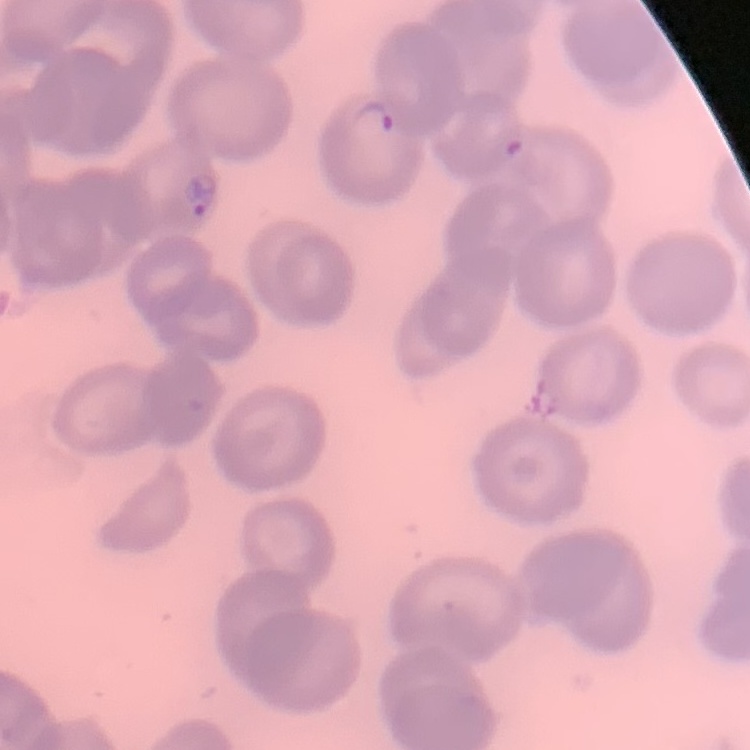

The erythrocytes show no rouleaux formation. Thin blood smear. One tile cut from a larger photomicrograph. Stained with either Field's or Giemsa.